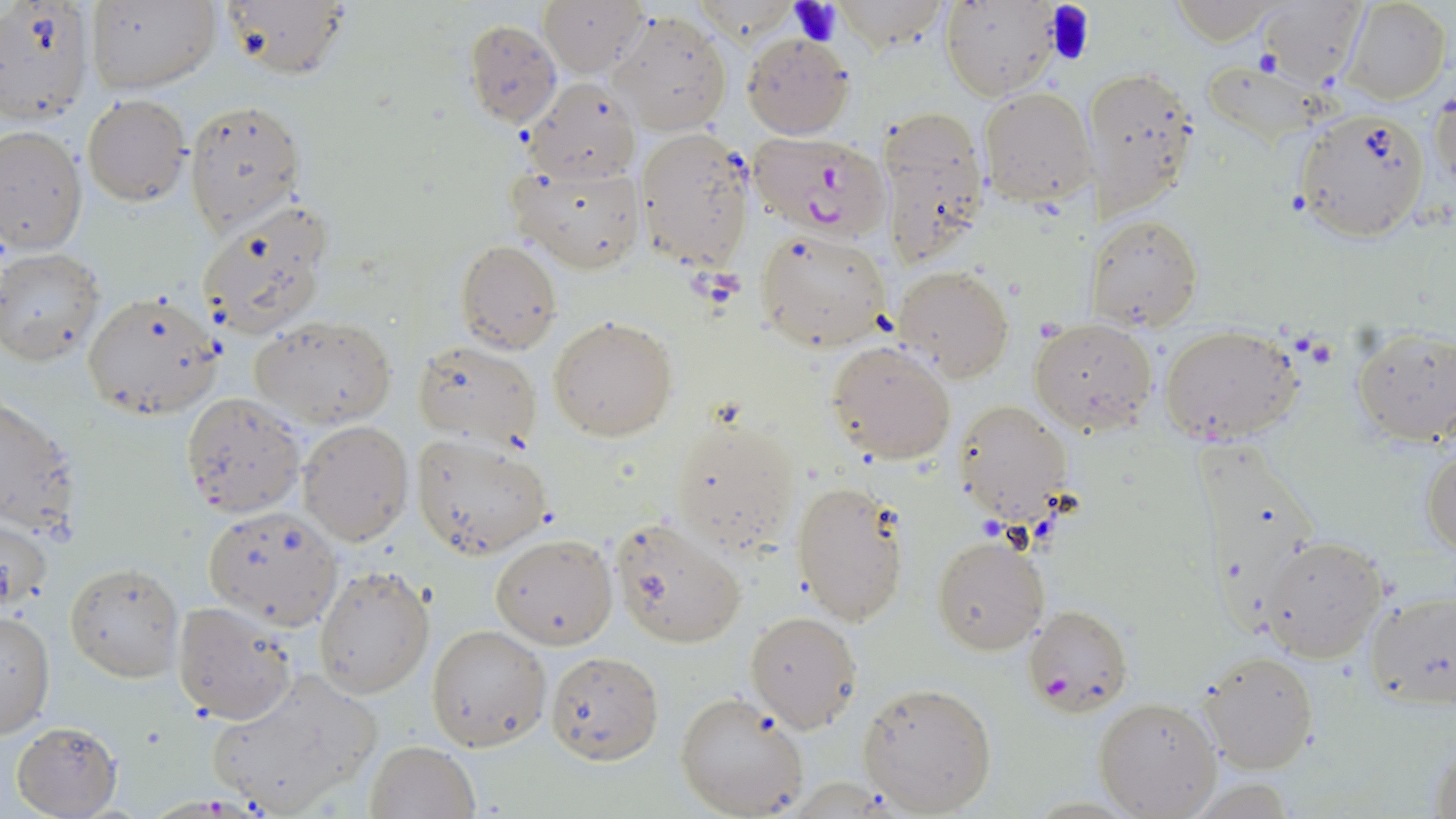
slide-level diagnosis = Plasmodium falciparum
stain = May-Grünwald-Giemsa
uninfected red blood cell locations = approximate bounding boxes as (x1,y1)-(x2,y2) corner pairs in pixels: (0,0)-(94,125), (86,0)-(222,92), (213,0)-(350,81), (943,1)-(1062,101), (1258,1)-(1368,86), (1341,1)-(1451,104), (539,2)-(648,78), (611,12)-(733,134), (463,18)-(562,128), (740,31)-(856,140), (1090,64)-(1201,223), (524,77)-(643,185), (1430,84)-(1455,205), (978,87)-(1097,207), (82,96)-(189,206), (183,99)-(302,231), (1292,106)-(1433,242), (875,108)-(990,269), (0,125)-(86,258), (635,127)-(756,272), (507,157)-(646,274), (196,205)-(333,341), (1089,211)-(1204,331), (755,226)-(891,352), (457,239)-(562,355), (1,249)-(104,365), (895,265)-(1013,383), (82,289)-(223,419), (251,315)-(396,429), (548,316)-(678,441), (1029,318)-(1159,434), (1158,325)-(1305,448), (1351,329)-(1456,447), (414,339)-(541,451), (826,339)-(956,463), (180,393)-(305,520), (1,394)-(80,538), (953,399)-(1071,523), (670,412)-(801,552), (298,419)-(414,547), (411,432)-(554,559), (1195,436)-(1318,633), (1422,441)-(1455,558), (791,478)-(908,626), (201,506)-(344,629), (2,514)-(54,613), (606,516)-(750,647), (490,533)-(617,649), (932,534)-(1050,656), (1259,536)-(1388,663), (64,561)-(183,682), (313,564)-(435,700), (1363,590)-(1455,710), (171,599)-(300,724), (0,609)-(55,739), (746,610)-(865,733), (426,625)-(550,752), (1197,648)-(1322,774), (546,650)-(664,764), (203,666)-(383,818), (858,681)-(998,815), (675,691)-(811,819), (1092,696)-(1222,818), (10,720)-(124,818), (1427,736)-(1455,818), (365,739)-(479,819)
modality = light microscopy
image size = 1456×819 pixels
platelet locations = approximate bounding boxes as (x1,y1)-(x2,y2) corner pairs in pixels: (789,0)-(846,45), (1043,1)-(1096,65), (1250,50)-(1284,78)
preparation = thin blood film
magnification = 1000x
Plasmodium falciparum-infected red blood cell locations = approximate bounding boxes as (x1,y1)-(x2,y2) corner pairs in pixels: (744,132)-(893,243), (1023,604)-(1133,718)
field of view = one of a larger specimen